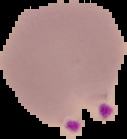
Image is 127×139 pixels. Cell region segmented out of the field of view; the surrounding area is masked to black. From a thin blood film. Result: Plasmodium parasites detected.